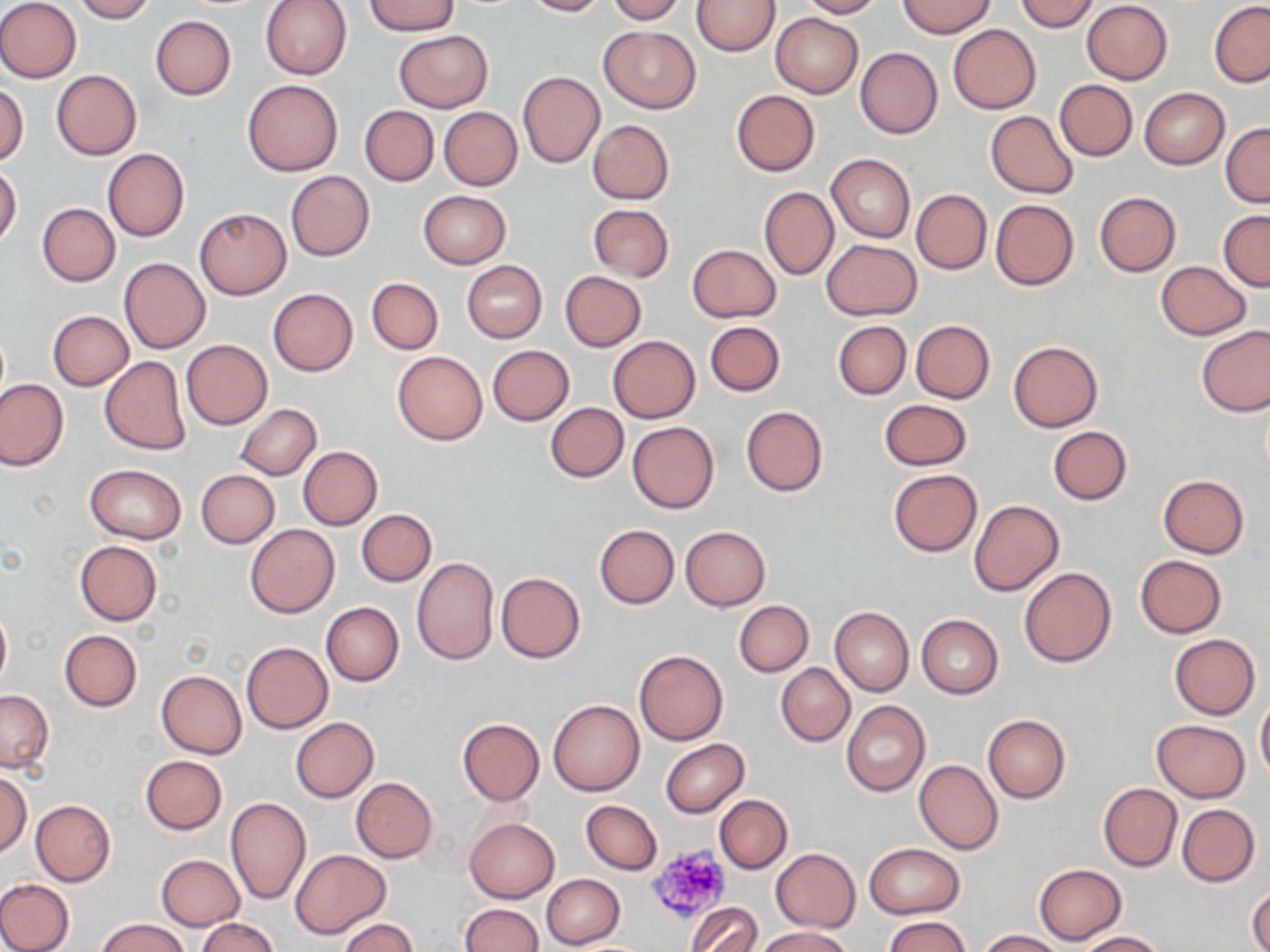
slide-level diagnosis = negative for blood parasites
uninfected red blood cell locations = approximate bounding boxes as named x1/y1/x2/y2 corners in pixels: (x1=0, y1=0, x2=81, y2=82), (x1=73, y1=0, x2=156, y2=23), (x1=260, y1=0, x2=352, y2=80), (x1=522, y1=0, x2=607, y2=17), (x1=605, y1=0, x2=684, y2=23), (x1=799, y1=0, x2=882, y2=18), (x1=897, y1=0, x2=995, y2=37), (x1=368, y1=1, x2=458, y2=35), (x1=693, y1=1, x2=779, y2=55), (x1=1016, y1=1, x2=1099, y2=32), (x1=1081, y1=1, x2=1173, y2=85), (x1=1209, y1=1, x2=1270, y2=87), (x1=770, y1=13, x2=863, y2=97), (x1=150, y1=15, x2=236, y2=100), (x1=947, y1=23, x2=1041, y2=113), (x1=600, y1=25, x2=699, y2=113), (x1=393, y1=30, x2=492, y2=113), (x1=854, y1=47, x2=942, y2=139), (x1=52, y1=69, x2=141, y2=160), (x1=517, y1=70, x2=604, y2=168), (x1=1054, y1=79, x2=1137, y2=161), (x1=242, y1=80, x2=343, y2=176), (x1=0, y1=82, x2=29, y2=166), (x1=1139, y1=88, x2=1229, y2=170), (x1=731, y1=89, x2=819, y2=176), (x1=359, y1=105, x2=438, y2=186), (x1=439, y1=107, x2=522, y2=190), (x1=986, y1=111, x2=1079, y2=198), (x1=588, y1=120, x2=674, y2=203), (x1=1221, y1=122, x2=1269, y2=207), (x1=103, y1=147, x2=188, y2=242), (x1=826, y1=153, x2=914, y2=242), (x1=0, y1=164, x2=22, y2=246), (x1=285, y1=170, x2=374, y2=261), (x1=759, y1=186, x2=838, y2=280), (x1=910, y1=189, x2=991, y2=275), (x1=418, y1=190, x2=511, y2=269), (x1=1093, y1=191, x2=1182, y2=277), (x1=990, y1=198, x2=1080, y2=291), (x1=37, y1=203, x2=120, y2=286), (x1=587, y1=203, x2=674, y2=282), (x1=195, y1=208, x2=291, y2=299), (x1=1218, y1=210, x2=1270, y2=290), (x1=821, y1=239, x2=922, y2=321), (x1=688, y1=244, x2=781, y2=322), (x1=119, y1=258, x2=210, y2=353), (x1=462, y1=261, x2=547, y2=343), (x1=1156, y1=261, x2=1250, y2=340), (x1=560, y1=271, x2=647, y2=352), (x1=367, y1=278, x2=443, y2=354), (x1=268, y1=288, x2=359, y2=377), (x1=48, y1=310, x2=133, y2=391), (x1=704, y1=320, x2=786, y2=397), (x1=833, y1=320, x2=911, y2=400), (x1=910, y1=320, x2=995, y2=403), (x1=1195, y1=325, x2=1269, y2=416), (x1=609, y1=336, x2=700, y2=423), (x1=181, y1=339, x2=272, y2=430), (x1=1007, y1=339, x2=1103, y2=432), (x1=487, y1=345, x2=574, y2=425), (x1=392, y1=351, x2=488, y2=445), (x1=100, y1=356, x2=192, y2=455), (x1=0, y1=378, x2=67, y2=471), (x1=878, y1=399, x2=972, y2=470), (x1=235, y1=403, x2=321, y2=479), (x1=545, y1=403, x2=628, y2=482), (x1=740, y1=405, x2=827, y2=496), (x1=627, y1=421, x2=718, y2=514), (x1=1048, y1=426, x2=1132, y2=505), (x1=297, y1=446, x2=382, y2=530), (x1=85, y1=464, x2=187, y2=543), (x1=888, y1=468, x2=981, y2=556), (x1=196, y1=469, x2=280, y2=547), (x1=1158, y1=475, x2=1249, y2=558), (x1=970, y1=500, x2=1063, y2=596), (x1=356, y1=509, x2=436, y2=587), (x1=245, y1=525, x2=339, y2=617), (x1=594, y1=525, x2=679, y2=609), (x1=679, y1=526, x2=770, y2=610), (x1=74, y1=540, x2=162, y2=626), (x1=1134, y1=555, x2=1227, y2=638), (x1=411, y1=557, x2=498, y2=664), (x1=1019, y1=567, x2=1116, y2=667), (x1=496, y1=571, x2=585, y2=662), (x1=734, y1=600, x2=812, y2=676), (x1=321, y1=602, x2=403, y2=686), (x1=0, y1=605, x2=11, y2=692), (x1=829, y1=606, x2=914, y2=696), (x1=916, y1=614, x2=1003, y2=698), (x1=60, y1=629, x2=141, y2=711), (x1=1168, y1=633, x2=1260, y2=720), (x1=242, y1=642, x2=333, y2=733), (x1=634, y1=650, x2=727, y2=744), (x1=776, y1=663, x2=854, y2=746), (x1=157, y1=670, x2=246, y2=759), (x1=0, y1=689, x2=53, y2=771), (x1=1255, y1=696, x2=1270, y2=783), (x1=549, y1=699, x2=645, y2=796), (x1=842, y1=701, x2=930, y2=797), (x1=982, y1=715, x2=1071, y2=803), (x1=291, y1=717, x2=379, y2=802), (x1=456, y1=718, x2=545, y2=805), (x1=1151, y1=719, x2=1250, y2=801), (x1=660, y1=739, x2=749, y2=817), (x1=140, y1=755, x2=228, y2=833), (x1=914, y1=759, x2=1002, y2=855), (x1=0, y1=772, x2=31, y2=857), (x1=350, y1=778, x2=437, y2=863), (x1=1098, y1=783, x2=1181, y2=872), (x1=714, y1=794, x2=792, y2=873), (x1=226, y1=797, x2=310, y2=905), (x1=30, y1=799, x2=115, y2=885), (x1=581, y1=800, x2=662, y2=875), (x1=1177, y1=804, x2=1260, y2=886), (x1=464, y1=816, x2=559, y2=903), (x1=863, y1=842, x2=966, y2=919), (x1=771, y1=848, x2=860, y2=932), (x1=291, y1=849, x2=390, y2=939), (x1=156, y1=854, x2=245, y2=931), (x1=1034, y1=863, x2=1125, y2=944), (x1=541, y1=873, x2=625, y2=948), (x1=0, y1=879, x2=74, y2=952), (x1=1248, y1=883, x2=1270, y2=952), (x1=458, y1=903, x2=543, y2=952), (x1=688, y1=903, x2=762, y2=952), (x1=882, y1=915, x2=972, y2=952), (x1=98, y1=917, x2=187, y2=952), (x1=195, y1=917, x2=278, y2=952), (x1=338, y1=917, x2=417, y2=952), (x1=755, y1=927, x2=852, y2=952), (x1=978, y1=930, x2=1063, y2=951), (x1=1076, y1=931, x2=1165, y2=951)
platelet locations = approximate bounding boxes as named x1/y1/x2/y2 corners in pixels: (x1=645, y1=843, x2=731, y2=924)
image size = 1270×952 pixels
field of view = one of a larger specimen
stain = May-Grünwald-Giemsa
modality = light microscopy
preparation = thin blood smear
magnification = 1000x